State the preparation type.
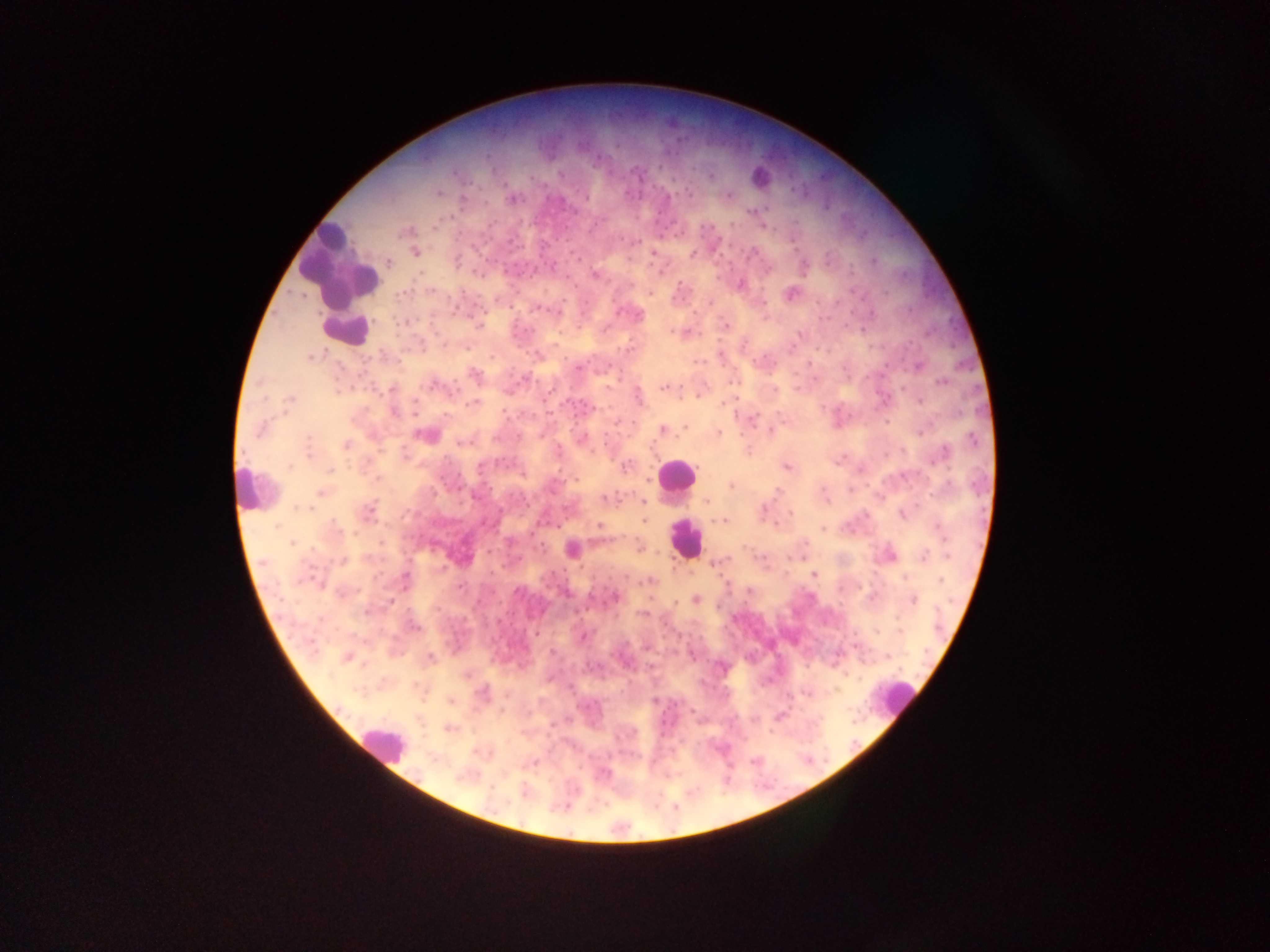
This is a thick smear.

Approximate centers as (x, y) in pixels.
Summary:
  - Plasmodium parasite locations: (560, 174), (711, 175), (439, 192), (728, 195), (586, 197), (463, 199), (513, 199), (407, 230), (415, 253), (654, 253), (693, 254), (388, 263), (553, 265), (481, 274), (595, 275), (740, 285), (431, 291), (403, 293), (650, 293), (790, 293), (710, 302), (538, 308), (479, 325), (726, 326), (800, 334), (628, 348), (467, 349), (720, 355), (311, 356), (918, 366), (578, 368), (475, 375), (525, 379), (942, 382), (433, 385), (663, 388), (392, 389), (639, 396), (290, 399), (885, 400), (919, 401), (473, 403), (393, 412), (751, 419), (686, 427), (260, 429), (662, 429), (771, 431), (719, 432), (920, 432), (426, 435), (973, 438), (309, 439), (582, 439), (460, 442), (346, 444), (943, 453), (290, 466), (626, 466), (786, 467), (331, 469), (731, 485), (321, 492), (604, 499), (707, 501), (643, 502), (299, 507), (764, 508), (370, 509), (791, 514), (904, 515), (646, 520), (720, 521), (599, 525), (336, 528), (823, 529), (940, 529), (291, 544), (890, 555), (924, 555), (566, 558), (342, 560), (714, 564), (813, 574), (405, 579), (940, 580), (650, 581), (460, 587), (565, 594), (616, 597), (696, 600), (913, 600), (390, 603), (676, 603), (414, 626), (583, 636), (552, 652), (346, 658), (430, 659), (450, 701), (448, 728), (534, 763), (605, 772)
  - Leukocyte locations: (762, 178), (340, 263), (346, 330), (675, 476), (250, 488), (684, 538), (897, 698), (382, 743)
  - Country: Ghana
  - Field of view: single
  - Capture: mobile-phone photograph through a microscope
  - Image size: 1270×952 pixels